Assess for malaria.
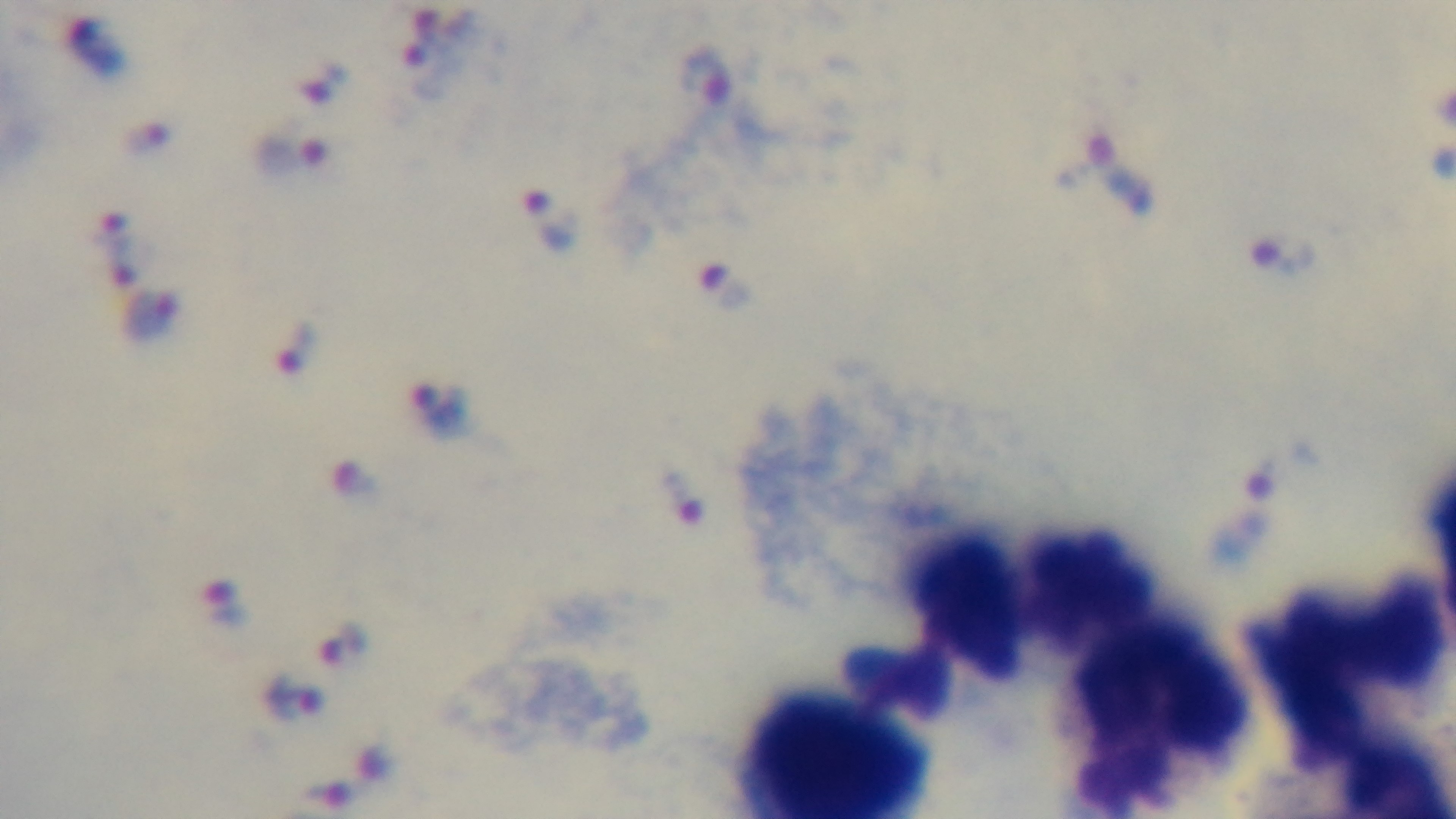
Positive.

Summary:
  - Field of view: one from the slide
  - Capture: mounted 4K digital camera
  - Stain: Giemsa
  - Modality: light microscopy
  - Objective: 100x oil immersion
  - Preparation: thick smear